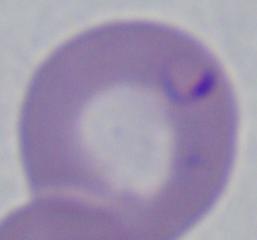 A Babesia parasite is shown. Photomicrograph. Captured at 1000x magnification.